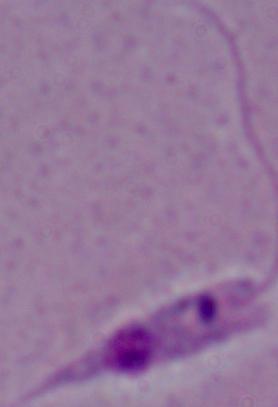

A Leishmania parasite is seen. Photomicrograph. Captured at 1000x magnification.